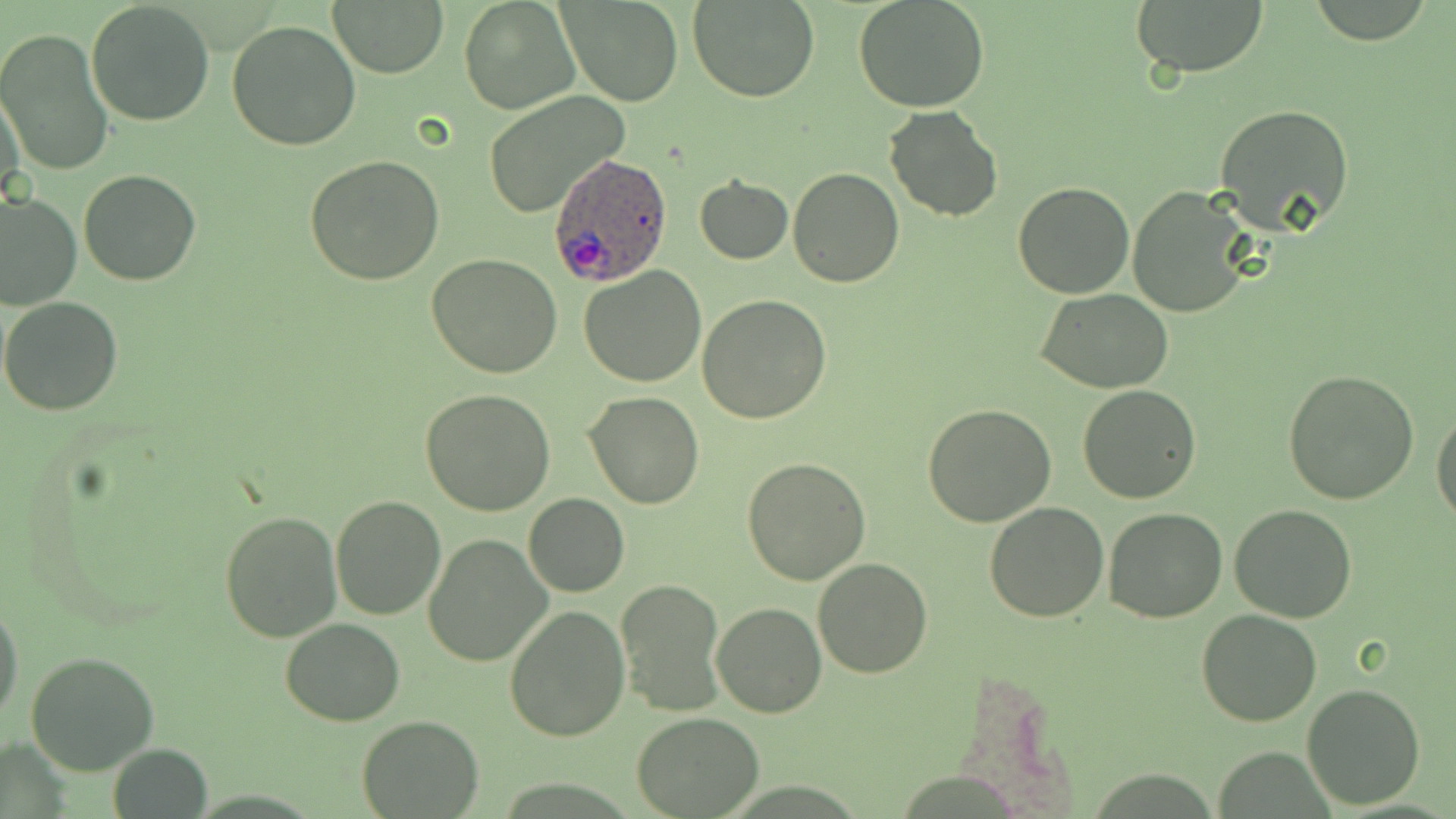 Approximate bounding boxes as (x1, y1, x2, y2) in pixels. Plasmodium ovale-infected red blood cell locations: (548, 151, 672, 290). Uninfected red blood cell locations: (86, 0, 216, 126), (559, 0, 683, 107), (689, 0, 821, 103), (853, 0, 990, 114), (1128, 0, 1270, 82), (459, 1, 577, 114), (330, 2, 448, 77), (3, 16, 202, 151), (226, 19, 362, 152), (0, 28, 113, 177), (0, 85, 26, 213), (482, 94, 628, 215), (1214, 102, 1357, 233), (883, 106, 1003, 222), (304, 155, 445, 285), (788, 167, 904, 286), (78, 169, 202, 286), (694, 176, 794, 265), (1012, 181, 1136, 299), (1128, 184, 1255, 317), (0, 191, 80, 311), (427, 253, 563, 377), (579, 264, 708, 386), (1037, 289, 1172, 393), (698, 294, 832, 425), (1, 296, 123, 417), (1284, 369, 1419, 504), (1077, 383, 1202, 503), (420, 388, 554, 515), (584, 392, 704, 511), (922, 404, 1057, 528), (1432, 410, 1456, 526), (741, 457, 871, 585), (523, 493, 629, 597), (330, 495, 446, 622), (984, 502, 1110, 623), (1229, 504, 1359, 623), (1101, 508, 1227, 624), (219, 510, 343, 644), (423, 534, 551, 666), (812, 558, 933, 678), (616, 580, 725, 715), (1, 597, 23, 728), (712, 601, 827, 718), (504, 604, 632, 741), (1196, 610, 1323, 727), (281, 617, 403, 726), (26, 650, 160, 776), (1302, 682, 1425, 810), (633, 710, 764, 817), (358, 715, 485, 818), (107, 744, 212, 819). Slide-level diagnosis: Plasmodium ovale. 1000x magnification. Thin blood film. Single field of view. Image is 1456×819 pixels. Optical microscopy. May-Grünwald-Giemsa-stained preparation.